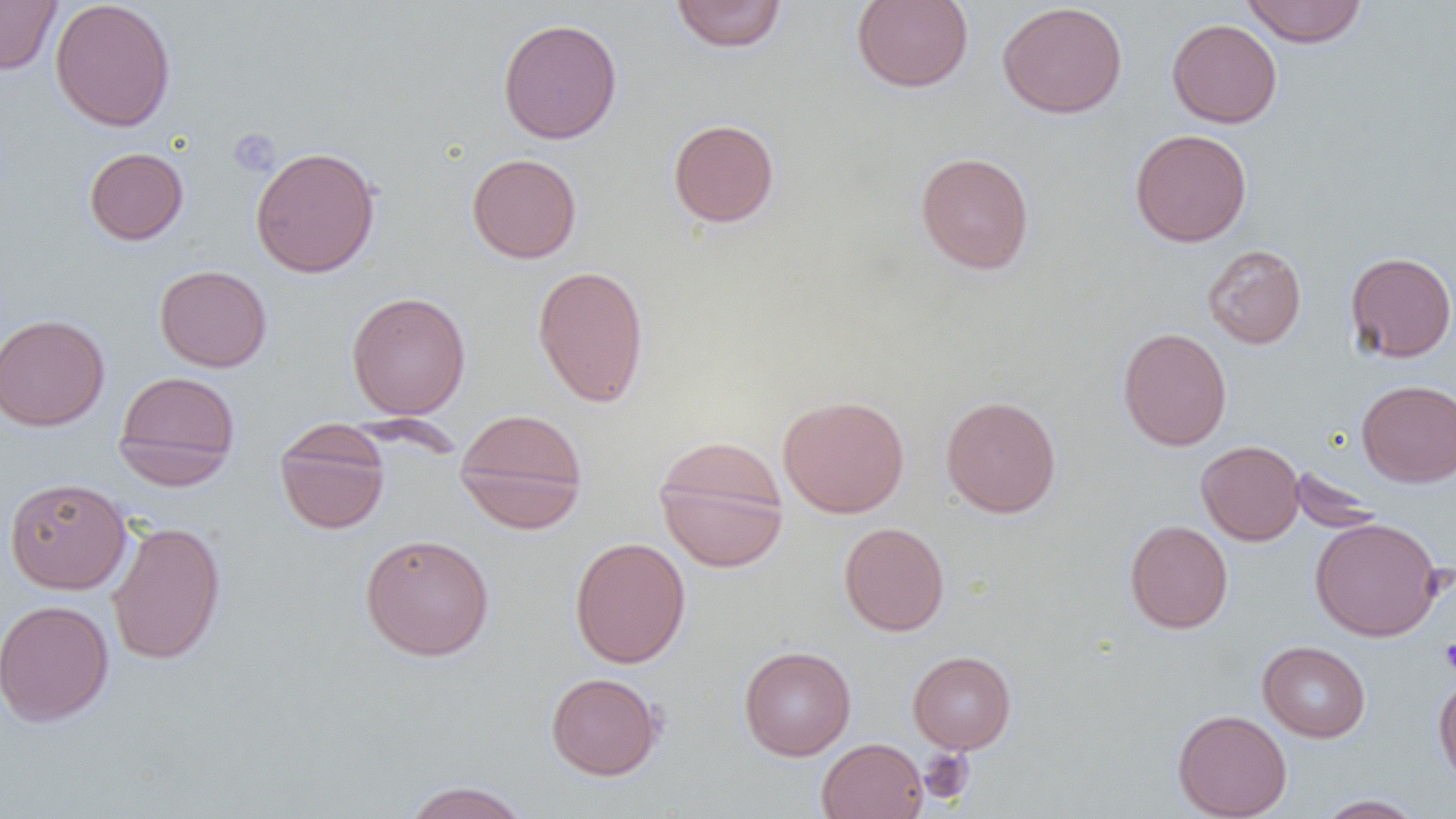 Approximate bounding boxes as [x1, y1, x2, y2] in pixels. Uninfected red blood cell locations: [0, 0, 61, 75], [50, 0, 176, 132], [852, 0, 974, 92], [1240, 0, 1369, 47], [670, 1, 787, 52], [997, 2, 1128, 119], [497, 17, 623, 144], [1167, 18, 1282, 128], [668, 118, 779, 227], [1130, 129, 1252, 247], [250, 146, 381, 278], [84, 147, 189, 245], [915, 151, 1034, 274], [467, 153, 582, 263], [1202, 244, 1307, 348], [1345, 251, 1456, 362], [154, 264, 272, 372], [532, 264, 650, 408], [346, 291, 471, 419], [0, 313, 110, 431], [1118, 327, 1232, 451], [113, 370, 241, 488], [1357, 380, 1456, 486], [777, 394, 910, 518], [941, 395, 1061, 518], [454, 406, 588, 533], [275, 421, 390, 535], [653, 437, 790, 573], [1196, 440, 1304, 545], [1290, 466, 1385, 533], [4, 477, 131, 594], [1310, 517, 1444, 641], [107, 520, 226, 666], [1124, 520, 1233, 634], [839, 521, 950, 636], [359, 533, 495, 660], [569, 536, 691, 668], [0, 599, 114, 727], [1258, 641, 1371, 742], [739, 645, 856, 760], [908, 650, 1016, 753], [545, 672, 665, 780], [1433, 673, 1456, 789], [1172, 709, 1292, 819], [817, 738, 927, 819], [401, 780, 533, 819], [1315, 794, 1425, 818]. Platelet locations: [228, 128, 281, 176], [1439, 636, 1456, 676], [917, 747, 974, 805]. Slide-level diagnosis: negative for blood parasites. Single field of view. Optical microscopy. Image is 1456×819 pixels. Thin blood film. Captured at 1000x magnification.